Report the malaria status of this cell.
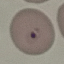
Parasitized.

Summary:
  - Image type: automatically extracted cell patch, resized to 64 × 64 pixels
  - Stain: Giemsa
  - Capture: smartphone through the microscope eyepiece
  - Preparation: thin blood smear